Comment on the morphology of the red blood cells.
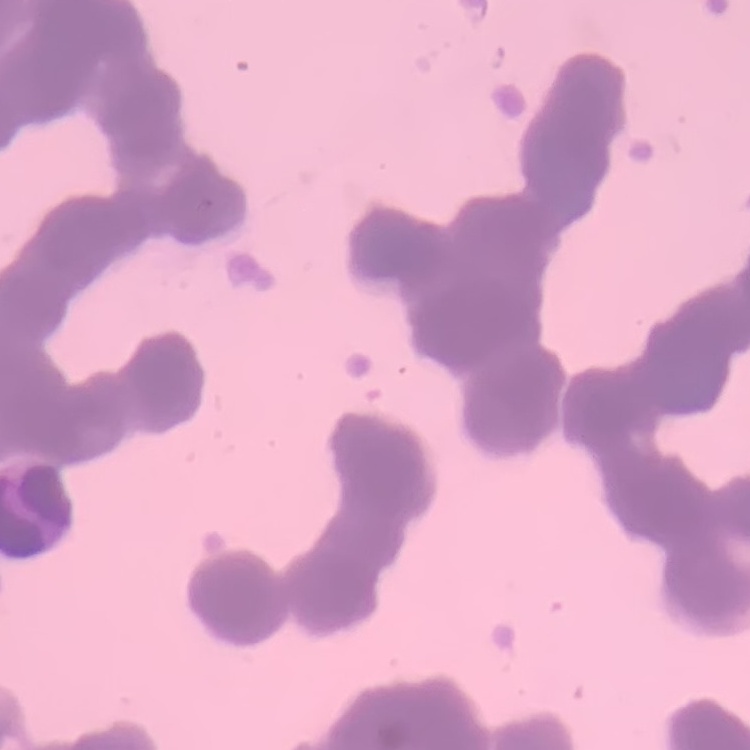

They show rouleaux formation.

preparation = thin blood film
image type = square crop of a larger photomicrograph
stain = Field's or Giemsa